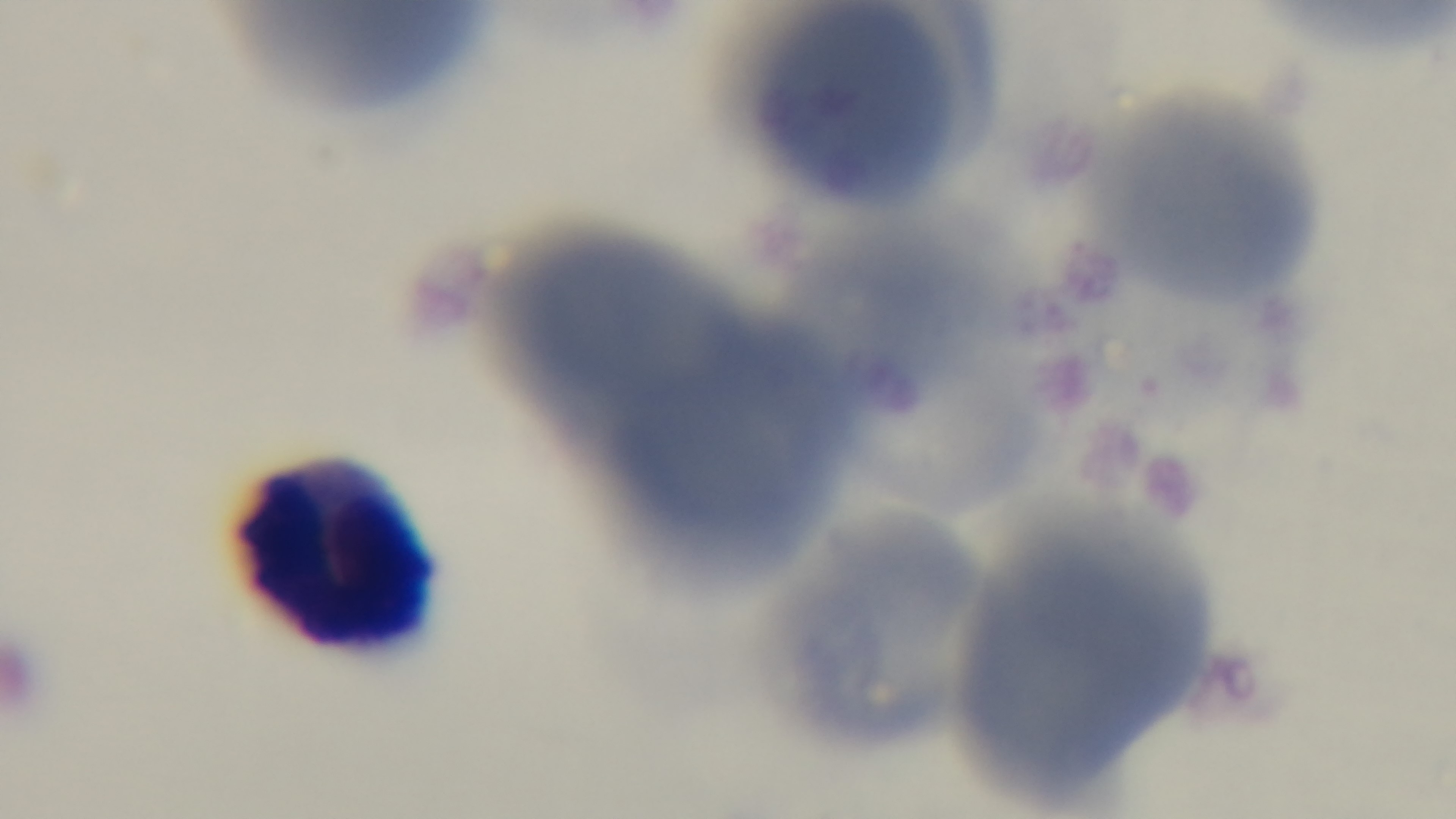
Mounted 4K digital camera. Malaria status: negative. Oil-immersion objective, 100x. Single field of view. Preparation: thin blood film. Light microscopy. Giemsa-stained.